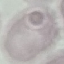
Summary:
  - Malaria status: uninfected
  - Capture: smartphone through the microscope eyepiece
  - Preparation: thin blood film
  - Stain: Giemsa
  - Image type: automatically extracted cell patch, resized to 64 × 64 pixels